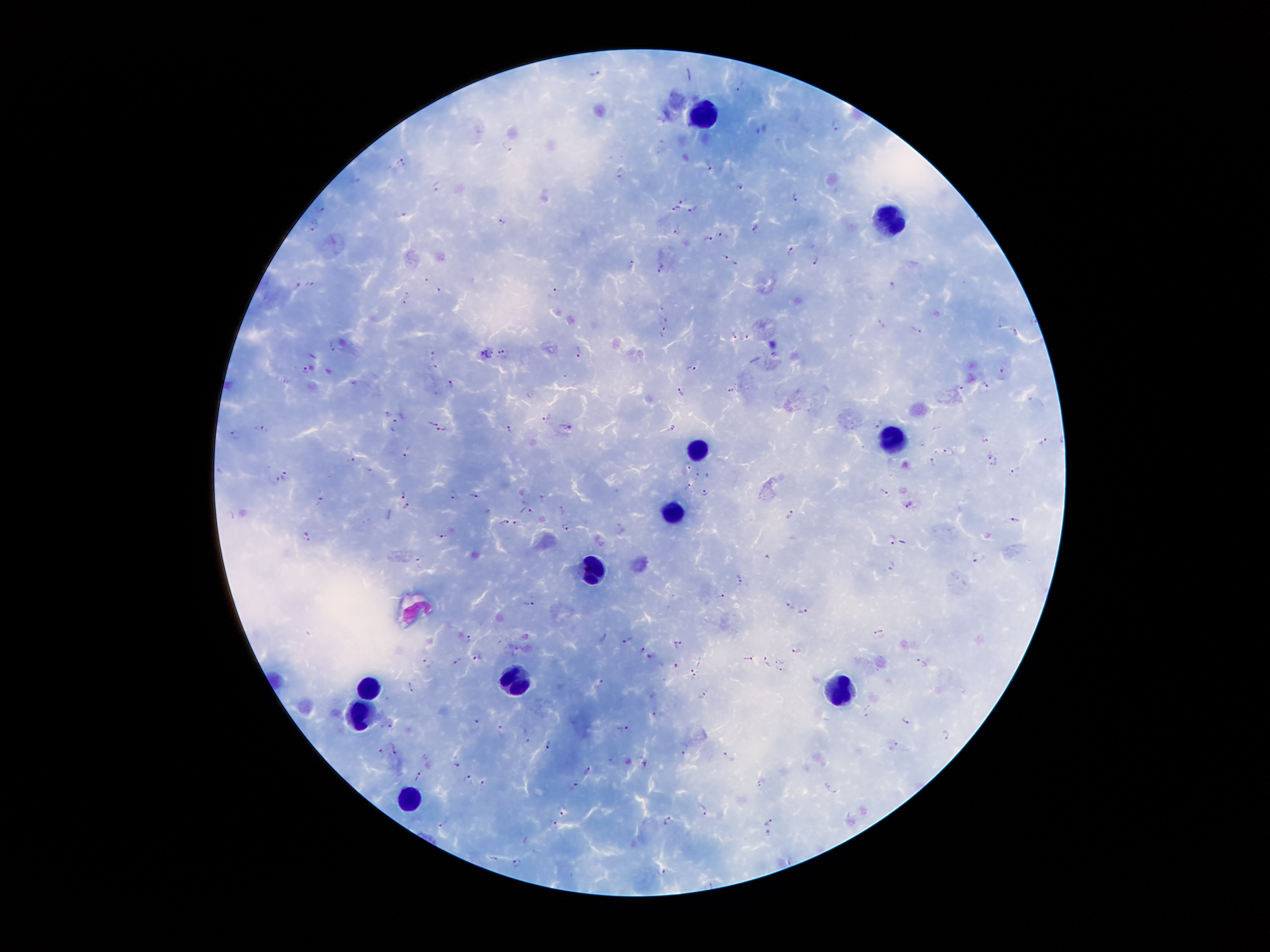

coordinate format = approximate centers as (x, y) in pixels
leukocyte locations = (707, 113), (889, 226), (898, 439), (698, 447), (674, 513), (590, 571), (518, 684), (373, 686), (848, 688), (364, 716), (405, 804)
malaria parasite locations = (595, 74), (742, 87), (838, 124), (507, 145), (402, 162), (710, 171), (621, 172), (740, 186), (437, 187), (682, 197), (795, 198), (322, 209), (676, 209), (696, 209), (403, 217), (501, 223), (317, 226), (754, 228), (677, 232), (722, 235), (707, 238), (790, 252), (725, 256), (815, 259), (631, 265), (661, 268), (427, 280), (312, 284), (298, 285), (893, 287), (439, 289), (554, 293), (407, 295), (402, 304), (661, 307), (665, 319), (881, 324), (916, 330), (664, 333), (1016, 333), (734, 335), (746, 336), (332, 344), (579, 351), (433, 352), (503, 354), (433, 365), (305, 368), (691, 369), (1003, 371), (451, 382), (985, 386), (959, 387), (731, 389), (681, 392), (386, 411), (546, 417), (398, 419), (433, 421), (880, 423), (672, 427), (510, 428), (259, 429), (570, 429), (442, 430), (236, 434), (984, 439), (1045, 441), (407, 450), (949, 450), (989, 453), (351, 460), (933, 462), (689, 464), (996, 465), (698, 472), (1013, 472), (286, 475), (273, 480), (690, 486), (884, 491), (704, 493), (405, 494), (452, 494), (476, 496), (543, 498), (321, 501), (909, 503), (405, 506), (562, 509), (526, 510), (791, 514), (232, 517), (1014, 520), (504, 521), (517, 523), (567, 527), (620, 528), (307, 536), (441, 536), (891, 538), (421, 559), (978, 561), (892, 566), (741, 580), (721, 593), (528, 604), (789, 605), (803, 610), (879, 632), (467, 638), (605, 638), (627, 639), (677, 644), (642, 647), (517, 648), (797, 650), (478, 655), (652, 656), (746, 659), (764, 660), (777, 660), (458, 661), (696, 661), (427, 662), (923, 663), (676, 665), (781, 671), (697, 676), (599, 684), (411, 687), (703, 694), (653, 695), (868, 711), (657, 714), (477, 720), (905, 720), (390, 723), (500, 729), (626, 731), (947, 736), (524, 740), (893, 745), (547, 746), (393, 749), (684, 750), (380, 751), (729, 757), (458, 762), (612, 762), (589, 771), (419, 773), (467, 777), (482, 783), (573, 783), (761, 783), (832, 789), (562, 809), (704, 810), (668, 821), (445, 822), (769, 822), (554, 823), (769, 833), (516, 862), (660, 870)
magnification = 100x
image size = 1270×952 pixels
field of view = one from this slide
patient malaria status = positive for Plasmodium falciparum
stain = Giemsa
preparation = thick blood smear
capture = smartphone camera through the microscope eyepiece